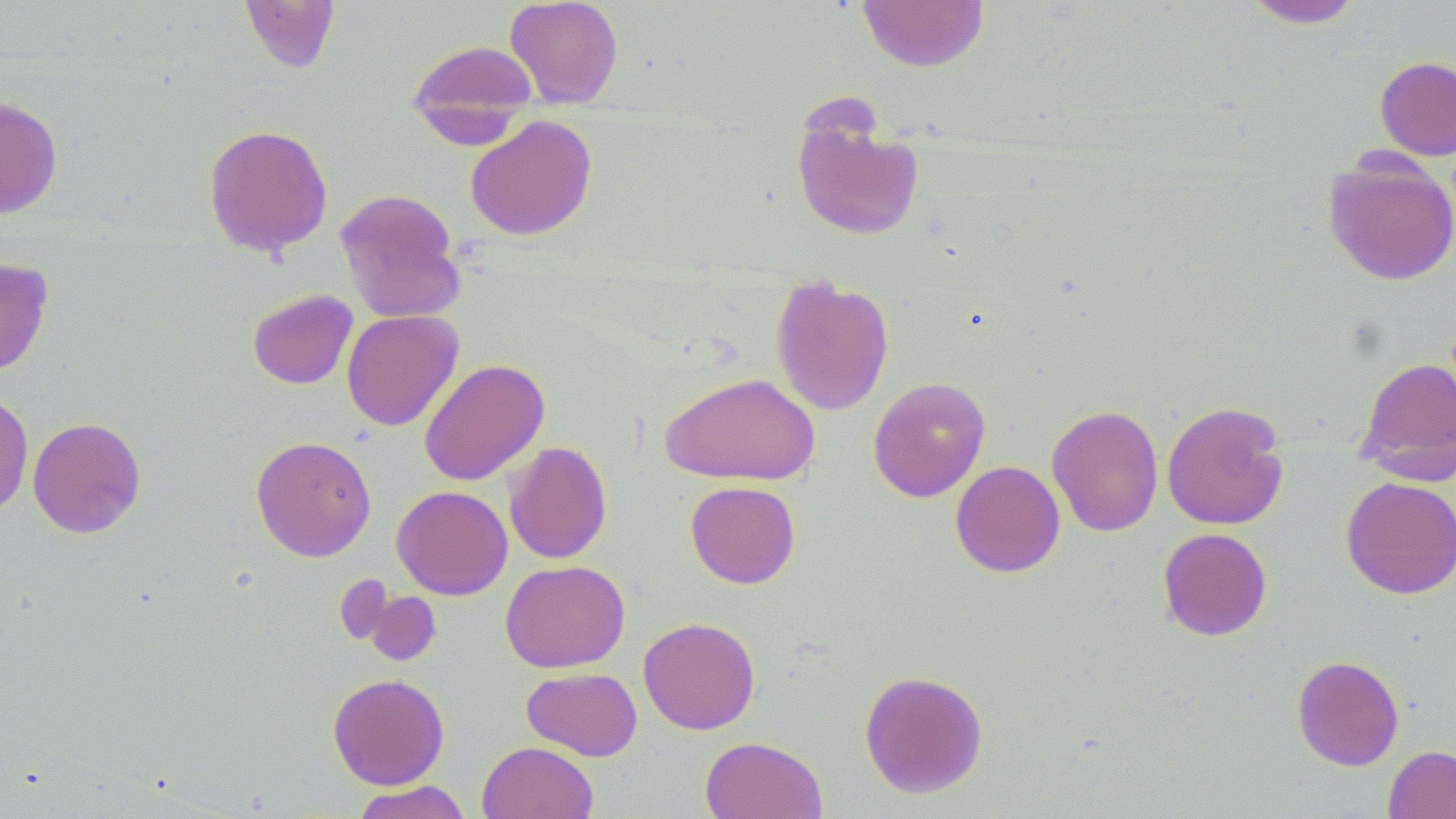
slide-level diagnosis = negative for blood parasites
modality = optical microscopy
preparation = thin blood smear
image size = 1456×819 pixels
uninfected red blood cell locations = approximate bounding boxes as (x1,y1)-(x2,y2) corner pairs in pixels: (504,0)-(624,109), (857,0)-(990,72), (1241,0)-(1365,28), (240,1)-(340,73), (406,38)-(539,143), (1374,56)-(1456,161), (0,96)-(63,220), (465,114)-(598,241), (793,115)-(924,241), (202,123)-(334,258), (1323,155)-(1456,287), (335,188)-(467,323), (0,258)-(53,378), (769,273)-(894,416), (246,288)-(358,390), (341,310)-(463,432), (1356,355)-(1456,468), (418,358)-(550,486), (659,371)-(820,486), (868,376)-(991,502), (0,389)-(34,519), (1162,400)-(1290,531), (1046,404)-(1164,537), (27,416)-(146,539), (250,436)-(377,562), (503,441)-(612,564), (950,460)-(1065,578), (1339,476)-(1456,599), (685,481)-(801,588), (391,485)-(512,600), (1157,528)-(1272,641), (500,560)-(630,673), (334,573)-(395,648), (366,591)-(442,666), (638,616)-(761,734), (1291,654)-(1405,770), (521,667)-(643,761), (859,669)-(988,799), (327,673)-(450,789), (699,736)-(828,819), (477,741)-(598,819), (1383,745)-(1456,819), (351,780)-(473,819)
field of view = single
magnification = 1000x
stain = May-Grünwald-Giemsa